Classify this cell by malaria status.
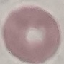

Uninfected.

stain = Giemsa
preparation = thin blood film
image type = automatically extracted cell patch, resized to 64 × 64 pixels
capture = smartphone camera at the microscope eyepiece